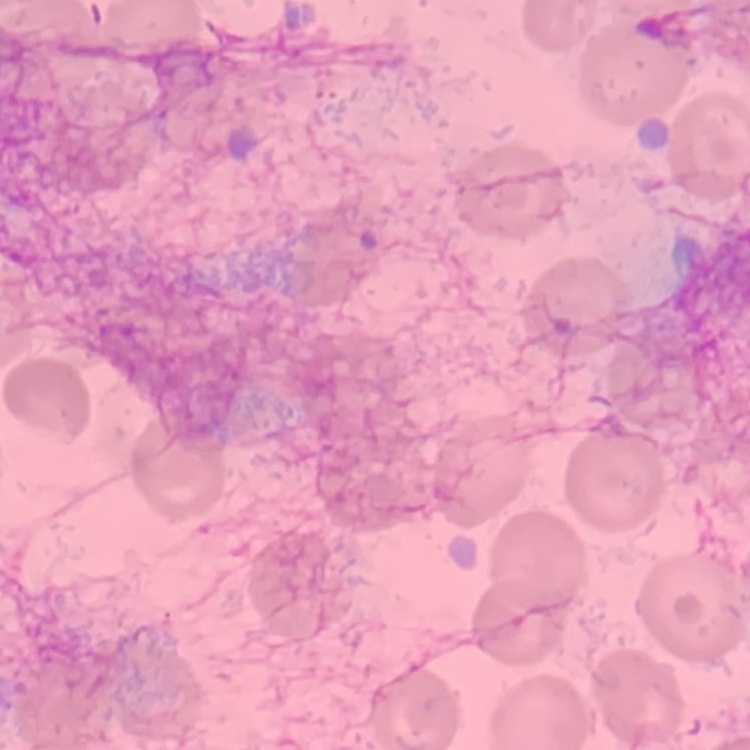
Summary:
  - Red blood cell morphology: no rouleaux formation
  - Stain: Field's or Giemsa
  - Image type: one tile cut from a larger photomicrograph
  - Preparation: thin peripheral smear